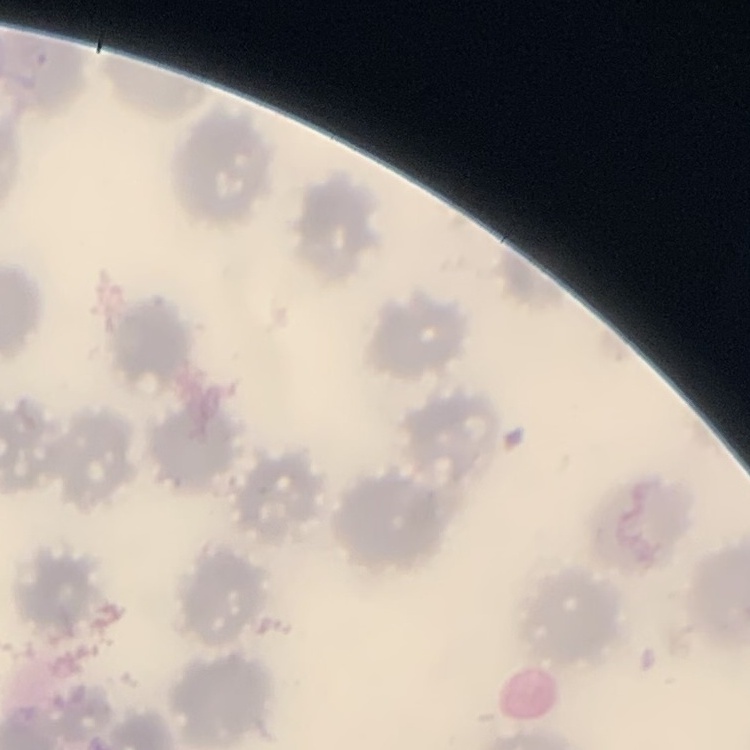
Summary:
  - Erythrocyte morphology: no rouleaux formation
  - Image type: one tile cut from a larger photomicrograph
  - Stain: Field's or Giemsa
  - Preparation: thin blood film